Report the malaria status of this cell.
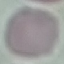
Uninfected.

Summary:
  - Stain: Giemsa
  - Image type: cell patch, automatically extracted from a larger field of view and resized to 64 × 64 pixels
  - Capture: smartphone camera at the microscope eyepiece
  - Preparation: thin smear